State which cell type is depicted.
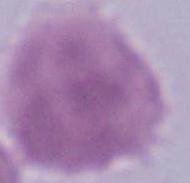

This is an erythrocyte.

Summary:
  - Modality: micrograph
  - Magnification: 1000x